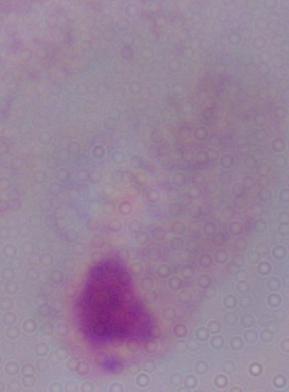

Summary:
  - Identification: trichomonad
  - Modality: photomicrograph
  - Magnification: 1000x